Locate every blood parasite and identify its species.
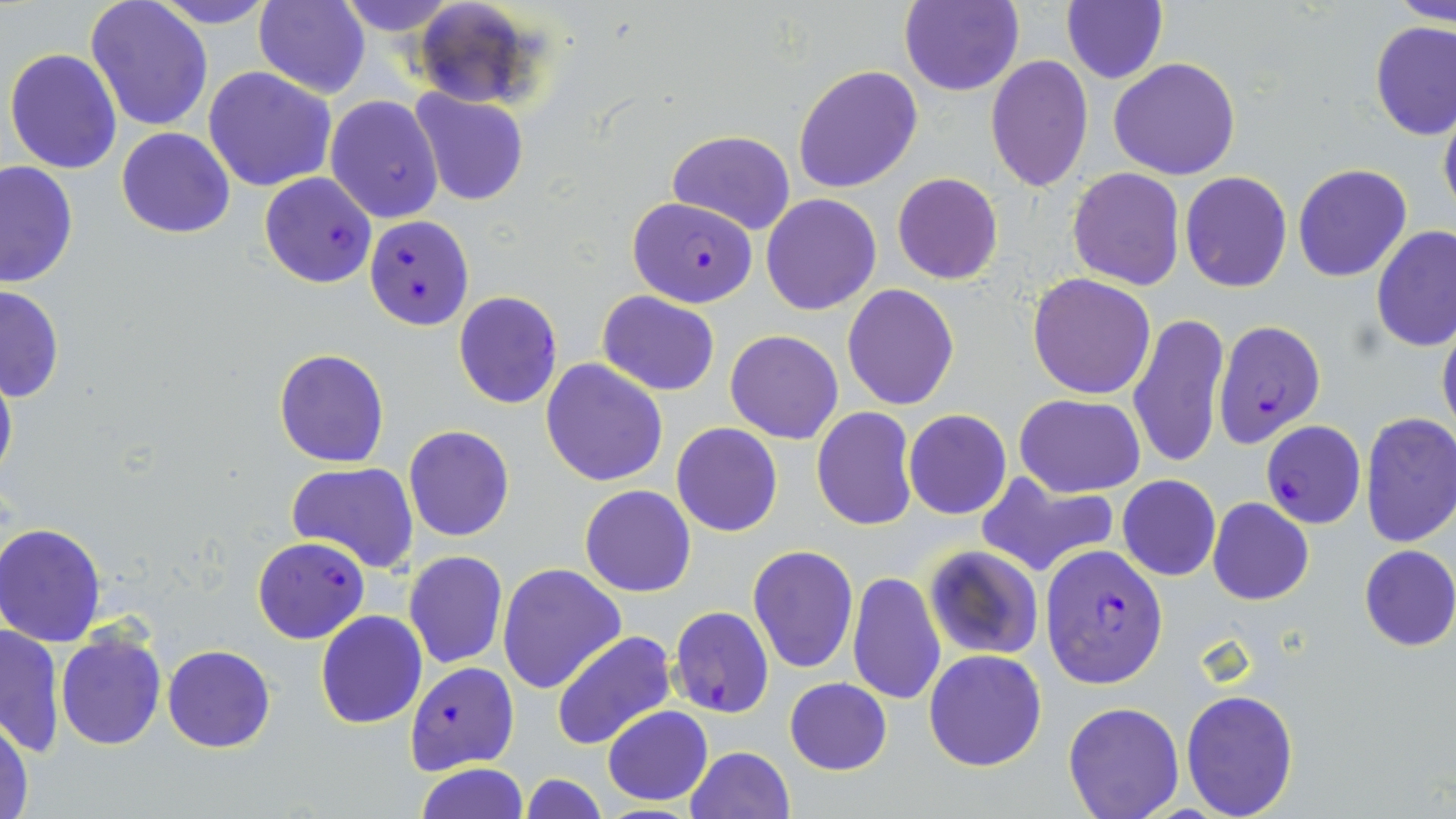

Approximate bounding boxes as [x1, y1, x2, y2] in pixels.
Plasmodium falciparum-infected red blood cells: [258, 172, 377, 287], [628, 197, 757, 307], [366, 214, 474, 331], [1213, 320, 1326, 448], [1261, 421, 1367, 529], [252, 537, 369, 644], [1039, 543, 1167, 688], [669, 606, 775, 719], [404, 661, 519, 774].
No Plasmodium ovale, Plasmodium malariae, Plasmodium vivax, Babesia divergens, or Trypanosoma brucei observed.

Summary:
  - Uninfected red blood cell locations: [148, 0, 280, 28], [253, 0, 371, 98], [333, 0, 461, 33], [899, 0, 1023, 96], [1390, 0, 1456, 24], [85, 1, 214, 132], [409, 1, 538, 106], [1062, 2, 1167, 83], [1369, 22, 1456, 140], [3, 47, 123, 175], [985, 55, 1095, 193], [1107, 57, 1241, 180], [794, 63, 923, 194], [203, 66, 336, 191], [410, 88, 530, 206], [326, 94, 444, 223], [1438, 96, 1456, 225], [116, 127, 235, 238], [666, 130, 796, 236], [1, 160, 78, 290], [1292, 163, 1413, 282], [1067, 168, 1184, 290], [1180, 171, 1292, 292], [891, 172, 1003, 284], [761, 193, 882, 315], [1371, 225, 1456, 352], [1027, 271, 1155, 399], [842, 283, 958, 409], [0, 284, 63, 402], [453, 290, 563, 409], [598, 291, 720, 396], [1128, 311, 1230, 471], [1437, 313, 1456, 443], [725, 330, 843, 444], [273, 348, 390, 469], [541, 358, 669, 486], [0, 360, 17, 490], [1015, 393, 1145, 495], [811, 407, 919, 531], [903, 409, 1012, 519], [1360, 412, 1456, 548], [671, 422, 783, 538], [403, 425, 514, 542], [285, 463, 420, 572], [977, 472, 1120, 577], [1117, 475, 1221, 581], [580, 484, 696, 598], [1118, 486, 1311, 592], [1207, 498, 1313, 606], [1, 524, 110, 646], [747, 544, 859, 674], [922, 544, 1045, 661], [1357, 545, 1456, 651], [403, 550, 508, 670], [497, 563, 626, 693], [848, 571, 946, 706], [315, 611, 428, 729], [0, 623, 65, 758], [56, 631, 167, 750], [550, 631, 676, 751], [163, 644, 275, 751], [924, 649, 1047, 772], [785, 679, 892, 775], [1180, 689, 1300, 818], [1062, 701, 1184, 818], [602, 704, 714, 807], [0, 717, 34, 819], [684, 746, 796, 819], [416, 764, 528, 819], [522, 772, 606, 819]
  - Slide-level diagnosis: Plasmodium falciparum
  - Field of view: single
  - Image size: 1456×819 pixels
  - Magnification: 1000x
  - Preparation: thin blood film
  - Stain: May-Grünwald-Giemsa
  - Modality: light microscopy